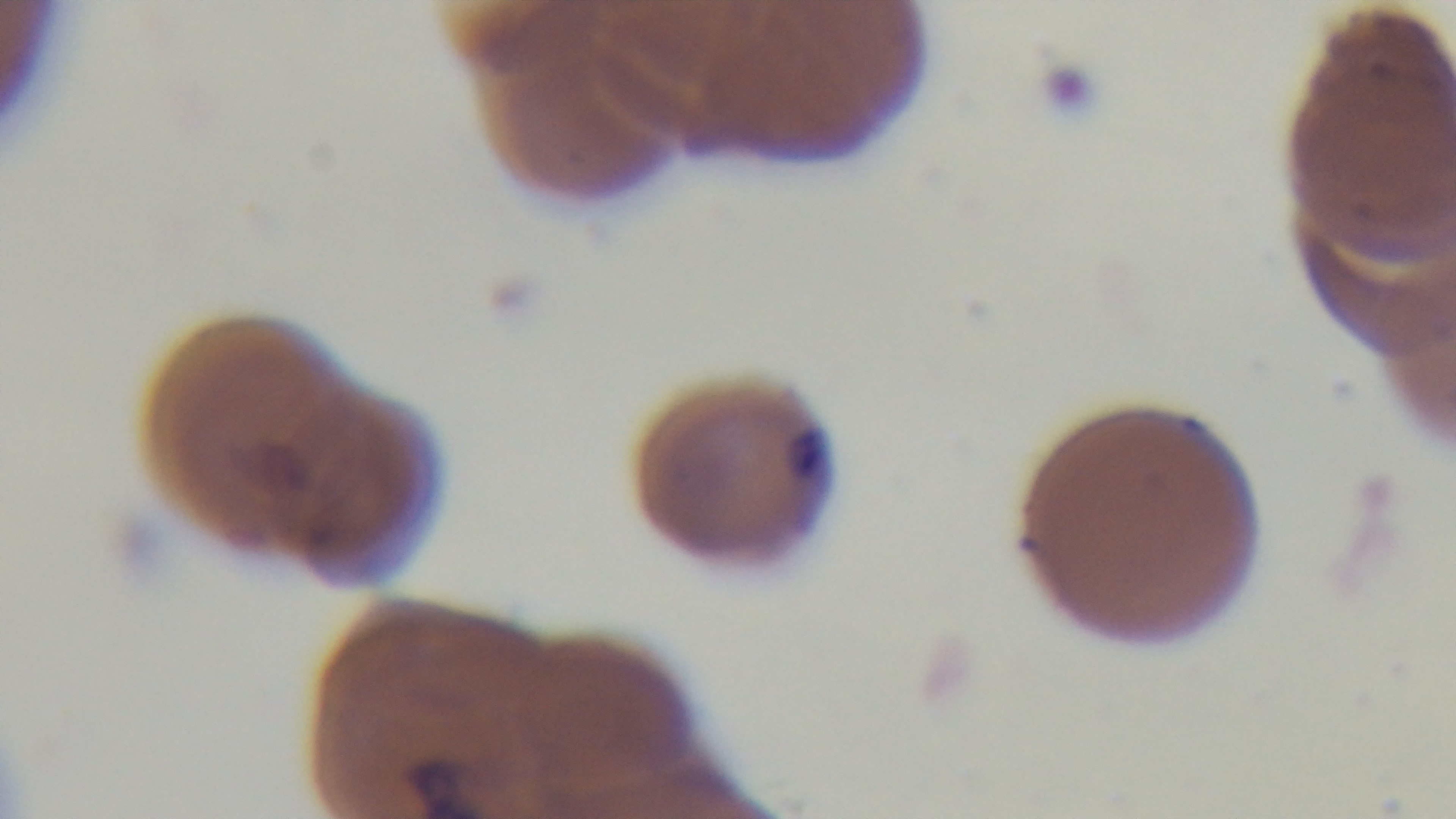

Summary:
  - Malaria status: infected
  - Modality: light microscopy
  - Stain: Giemsa
  - Preparation: thin smear
  - Objective: 100x oil immersion
  - Capture: mounted 4K digital camera
  - Field of view: one from the slide